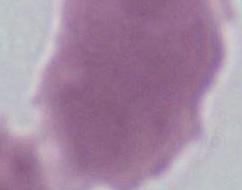

magnification = 1000x
identification = erythrocyte
modality = photomicrograph